Assess this cell for malaria.
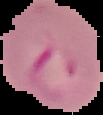

Parasitized.

image size = 103×115 pixels
preparation = thin blood smear
image type = cell region segmented out of the field of view; surrounding area masked to black